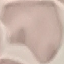
{
  "malaria_status": "uninfected",
  "stain": "Giemsa",
  "preparation": "thin blood smear",
  "image_type": "cell patch, automatically extracted from a larger field of view and resized to 64 × 64 pixels",
  "capture": "smartphone through the microscope eyepiece"
}